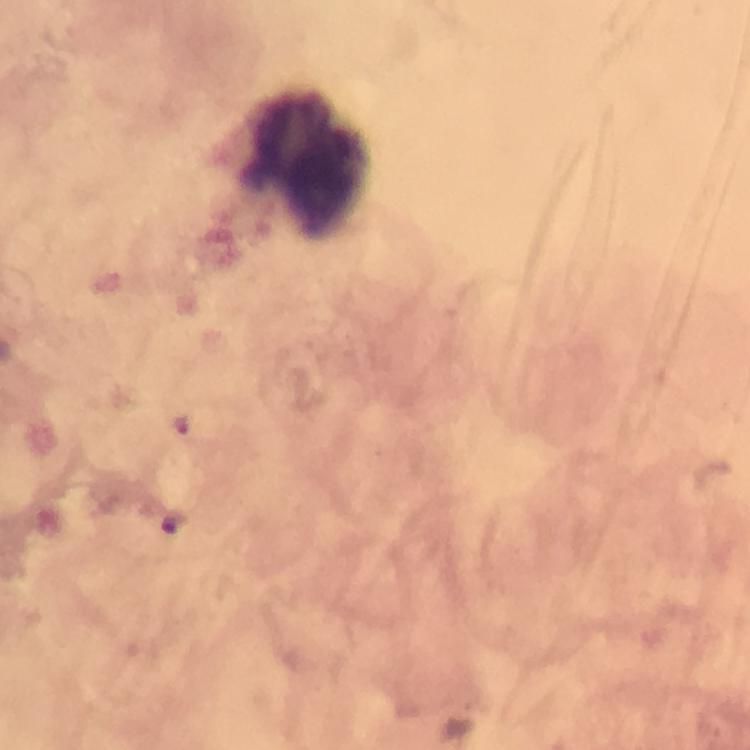 Approximate object centers, in pixels from the top-left corner. Leukocyte locations: (x=302, y=162). 100x magnification. Thick smear. Malaria parasites: none detected. Immersion oil applied. Giemsa-stained preparation. A crop from one field of view. From a diagnostic examination for malaria. Smartphone photograph taken through a microscope. Image is 750×750 pixels.